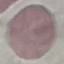
result = no malaria parasites seen
image type = automatically extracted cell patch, resized to 64 × 64 pixels
capture = smartphone through the microscope eyepiece
stain = Giemsa
preparation = thin blood smear